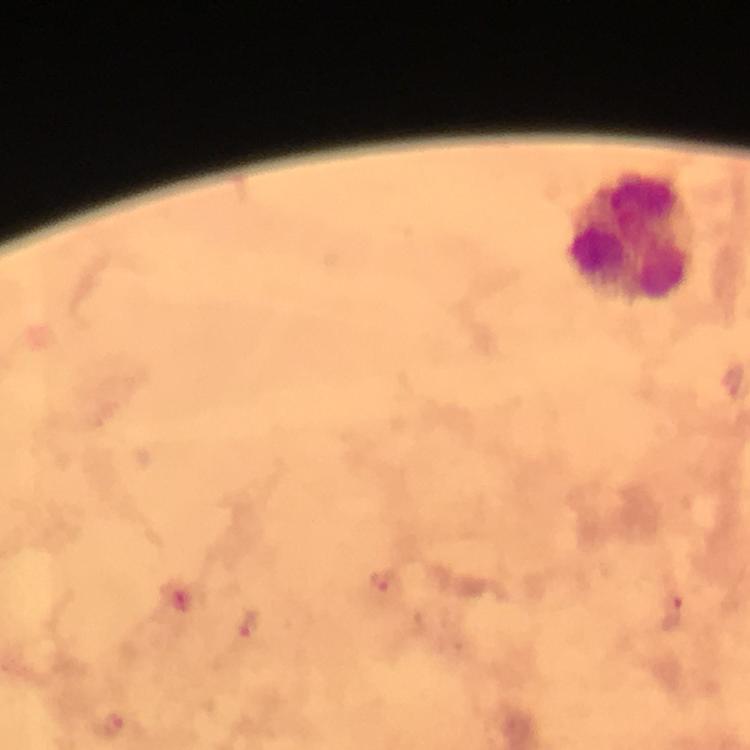
leukocyte locations = approximate centers as {x, y} in pixels: {632, 236}
magnification = 100x
Plasmodium parasite locations = approximate centers as {x, y} in pixels: {384, 587}, {672, 608}, {247, 627}, {112, 725}
preparation = thick smear
cropped from = a single field of view
stain = Giemsa
context = from a diagnostic examination for malaria
capture = smartphone photograph through a microscope
immersion oil = applied
image size = 750×750 pixels